Assess this cell for malaria.
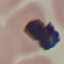
It is uninfected.

{
  "capture": "smartphone camera at the microscope eyepiece",
  "stain": "Giemsa",
  "image_type": "automatically extracted cell patch, resized to 64 × 64 pixels",
  "preparation": "thin blood smear"
}